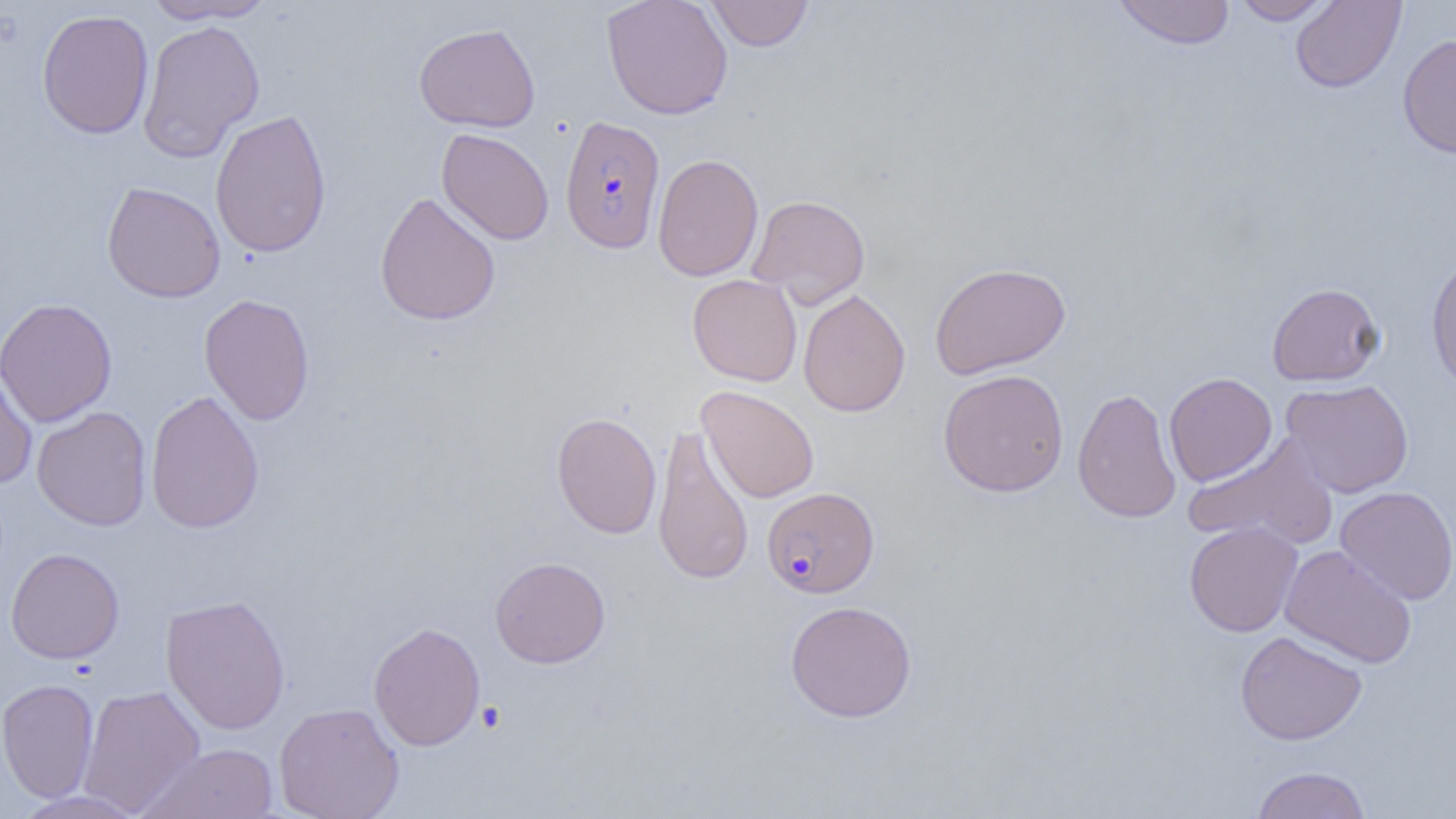

slide-level diagnosis = Plasmodium falciparum
magnification = 1000x
uninfected red blood cell locations = approximate bounding boxes as (x1,y1)-(x2,y2) corner pairs in pixels: (141,0)-(278,25), (601,0)-(733,120), (706,0)-(814,52), (1111,0)-(1236,49), (1230,0)-(1336,24), (1291,0)-(1407,93), (36,9)-(154,139), (138,18)-(265,161), (414,22)-(541,133), (1397,33)-(1456,158), (210,109)-(332,259), (436,127)-(554,245), (652,153)-(764,282), (101,181)-(226,303), (374,192)-(501,327), (747,194)-(871,306), (1425,254)-(1456,396), (929,261)-(1071,380), (687,274)-(802,387), (1266,282)-(1384,386), (797,289)-(911,418), (199,294)-(315,426), (0,297)-(117,427), (0,360)-(38,488), (938,368)-(1069,497), (1163,372)-(1277,486), (1280,378)-(1414,498), (697,385)-(819,503), (1072,387)-(1182,524), (145,389)-(265,535), (32,406)-(152,531), (551,412)-(662,539), (652,424)-(754,585), (1184,436)-(1338,549), (1335,486)-(1456,605), (1184,521)-(1303,637), (1280,544)-(1418,669), (5,547)-(125,664), (489,556)-(610,668), (160,593)-(291,735), (785,600)-(917,723), (368,621)-(486,751), (1235,630)-(1367,746), (0,678)-(99,803), (77,684)-(206,816), (274,701)-(404,819), (140,743)-(280,819), (1251,766)-(1370,817), (10,789)-(148,818)
modality = optical microscopy
platelet locations = approximate bounding boxes as (x1,y1)-(x2,y2) corner pairs in pixels: (476,701)-(507,733)
image size = 1456×819 pixels
field of view = one of a larger specimen
preparation = thin blood film
Plasmodium falciparum-infected red blood cell locations = approximate bounding boxes as (x1,y1)-(x2,y2) corner pairs in pixels: (560,115)-(666,254), (762,486)-(879,598)